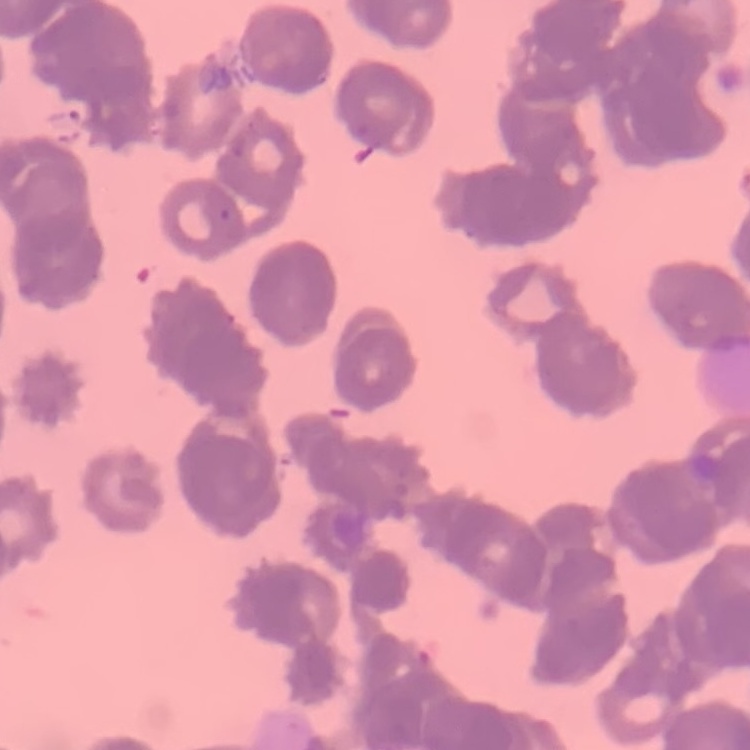

The erythrocytes exhibit rouleaux formation. Square crop of a larger photomicrograph. Field's or Giemsa stain. Thin blood film.